Describe the morphology of the erythrocytes.
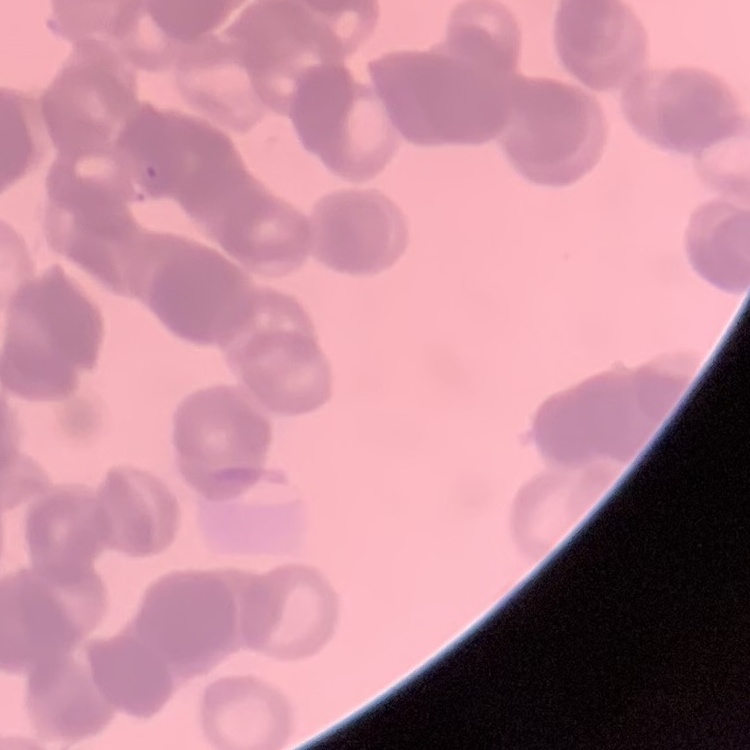
They show rouleaux formation.

Stained with either Field's or Giemsa. One tile cut from a larger photomicrograph. Thin blood film.